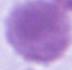

Summary:
  - Modality: micrograph
  - Magnification: 1000x
  - Identification: red blood cell